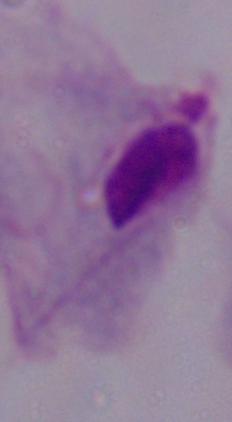

A trichomonad is shown. Micrograph. 1000x magnification.